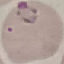

Summary:
  - Result: malaria parasites identified
  - Preparation: thin smear
  - Stain: Giemsa
  - Image type: automatically extracted cell patch, resized to 64 × 64 pixels
  - Capture: smartphone camera at the microscope eyepiece